Report the malaria status of this cell.
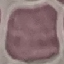
It is uninfected.

{
  "preparation": "thin smear",
  "capture": "smartphone camera at the microscope eyepiece",
  "stain": "Giemsa",
  "image_type": "cell patch, automatically extracted from a larger field of view and resized to 64 × 64 pixels"
}